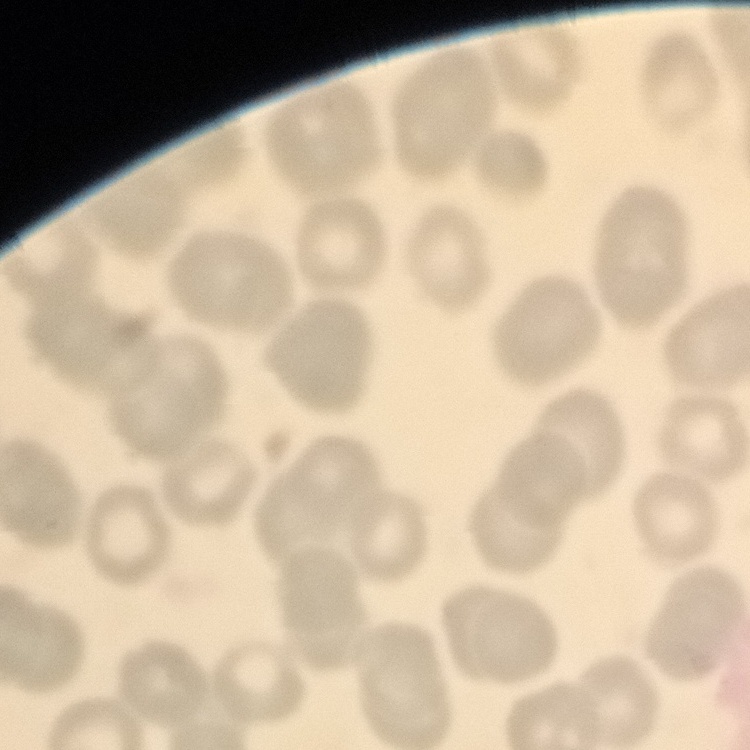

erythrocyte morphology = no rouleaux formation
stain = Field's or Giemsa
image type = one tile cut from a larger photomicrograph
preparation = thin blood film